Report the malaria status of this cell.
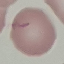
Uninfected.

Summary:
  - Stain: Giemsa
  - Capture: smartphone camera at the microscope eyepiece
  - Image type: automatically extracted cell patch, resized to 64 × 64 pixels
  - Preparation: thin blood film